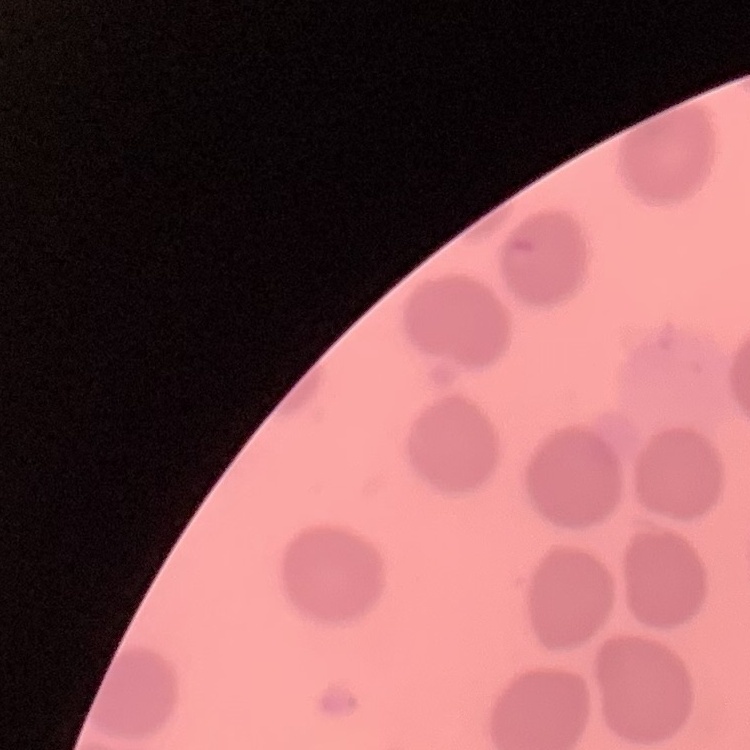

The erythrocytes exhibit no rouleaux formation. One tile cut from a larger photomicrograph. Field's or Giemsa stain. Thin blood smear.